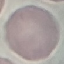
Malaria status: uninfected. Thin blood film. Acquired by smartphone through the microscope eyepiece. Giemsa-stained preparation. Automatically extracted cell patch, resized to 64 × 64 pixels.